Assess this cell for malaria.
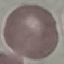

It is uninfected.

Automatically extracted cell patch, resized to 64 × 64 pixels. Photographed with a smartphone camera at the microscope eyepiece. Thin smear of blood. Giemsa stain.